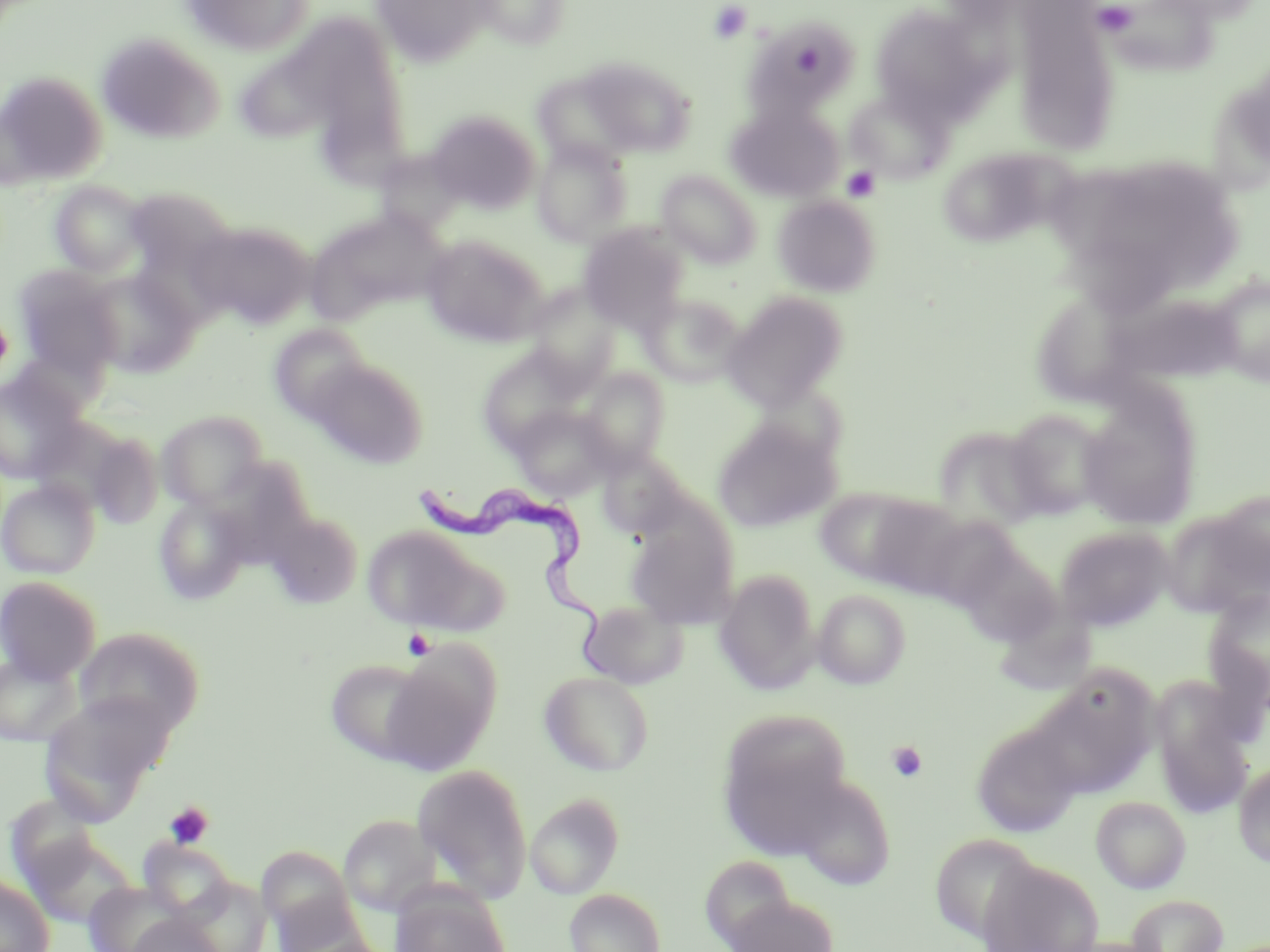

{
  "trypanosoma_brucei_locations": "approximate bounding boxes as (x1,y1)-(x2,y2) corner pairs in pixels: (415,474)-(623,674)",
  "slide_level_diagnosis": "Trypanosoma brucei",
  "preparation": "thin blood smear",
  "field_of_view": "single",
  "image_size": "1270×952 pixels",
  "uninfected_red_blood_cell_locations": "approximate bounding boxes as (x1,y1)-(x2,y2) corner pairs in pixels: (176,0)-(314,57), (371,0)-(498,67), (471,0)-(572,50), (1148,0)-(1264,23), (870,3)-(991,119), (1011,7)-(1122,154), (749,20)-(857,114), (282,23)-(403,121), (95,32)-(225,145), (583,59)-(697,156), (0,69)-(108,188), (531,70)-(642,171), (845,88)-(953,184), (725,100)-(845,202), (323,101)-(418,200), (427,109)-(541,214), (532,140)-(633,245), (938,147)-(1061,247), (1068,156)-(1247,303), (657,169)-(762,268), (49,181)-(148,276), (133,189)-(231,278), (773,195)-(881,297), (301,207)-(450,327), (188,220)-(316,329), (578,224)-(689,330), (420,233)-(550,347), (13,266)-(123,379), (85,267)-(198,377), (1209,276)-(1270,385), (523,287)-(622,390), (1037,287)-(1142,407), (721,291)-(849,411), (640,293)-(746,388), (1110,295)-(1251,392), (269,324)-(371,423), (476,347)-(585,453), (309,357)-(428,469), (579,369)-(670,471), (0,370)-(86,484), (1077,386)-(1203,529), (512,405)-(616,501), (1004,409)-(1109,520), (156,410)-(269,512), (712,419)-(839,534), (934,426)-(1048,532), (87,430)-(165,529), (596,451)-(691,539), (0,478)-(100,578), (817,486)-(949,590), (1213,489)-(1270,588), (154,495)-(250,605), (263,509)-(363,609), (924,510)-(1014,616), (1159,512)-(1268,620), (626,518)-(739,629), (1054,525)-(1174,630), (362,526)-(479,630), (715,568)-(820,693), (0,575)-(102,683), (813,589)-(910,689), (1203,589)-(1270,711), (578,599)-(688,690), (994,609)-(1104,693), (73,627)-(205,734), (0,648)-(84,747), (380,652)-(497,774), (324,658)-(432,764), (539,669)-(654,776), (1025,672)-(1158,800), (1152,685)-(1255,820), (39,691)-(175,823), (717,711)-(856,853), (971,722)-(1083,838), (412,762)-(535,905), (1233,762)-(1270,868), (792,772)-(896,891), (525,792)-(624,898), (1091,795)-(1191,893), (338,814)-(441,917), (25,832)-(139,928), (930,833)-(1040,944), (139,839)-(237,921), (257,845)-(356,937), (699,854)-(797,948), (976,857)-(1105,952), (0,875)-(55,952), (178,878)-(272,952), (82,881)-(192,952), (389,887)-(511,952), (564,888)-(665,952), (725,892)-(839,952), (1126,893)-(1228,952), (271,901)-(378,952), (124,914)-(226,952)",
  "stain": "May-Grünwald-Giemsa",
  "magnification": "1000x",
  "modality": "light microscopy",
  "platelet_locations": "approximate bounding boxes as (x1,y1)-(x2,y2) corner pairs in pixels: (708,2)-(752,43), (1091,2)-(1138,37), (842,166)-(879,202), (0,308)-(12,381), (403,629)-(436,660), (887,741)-(927,783), (164,802)-(214,849)"
}